Give the position of every Plasmodium parasite visible.
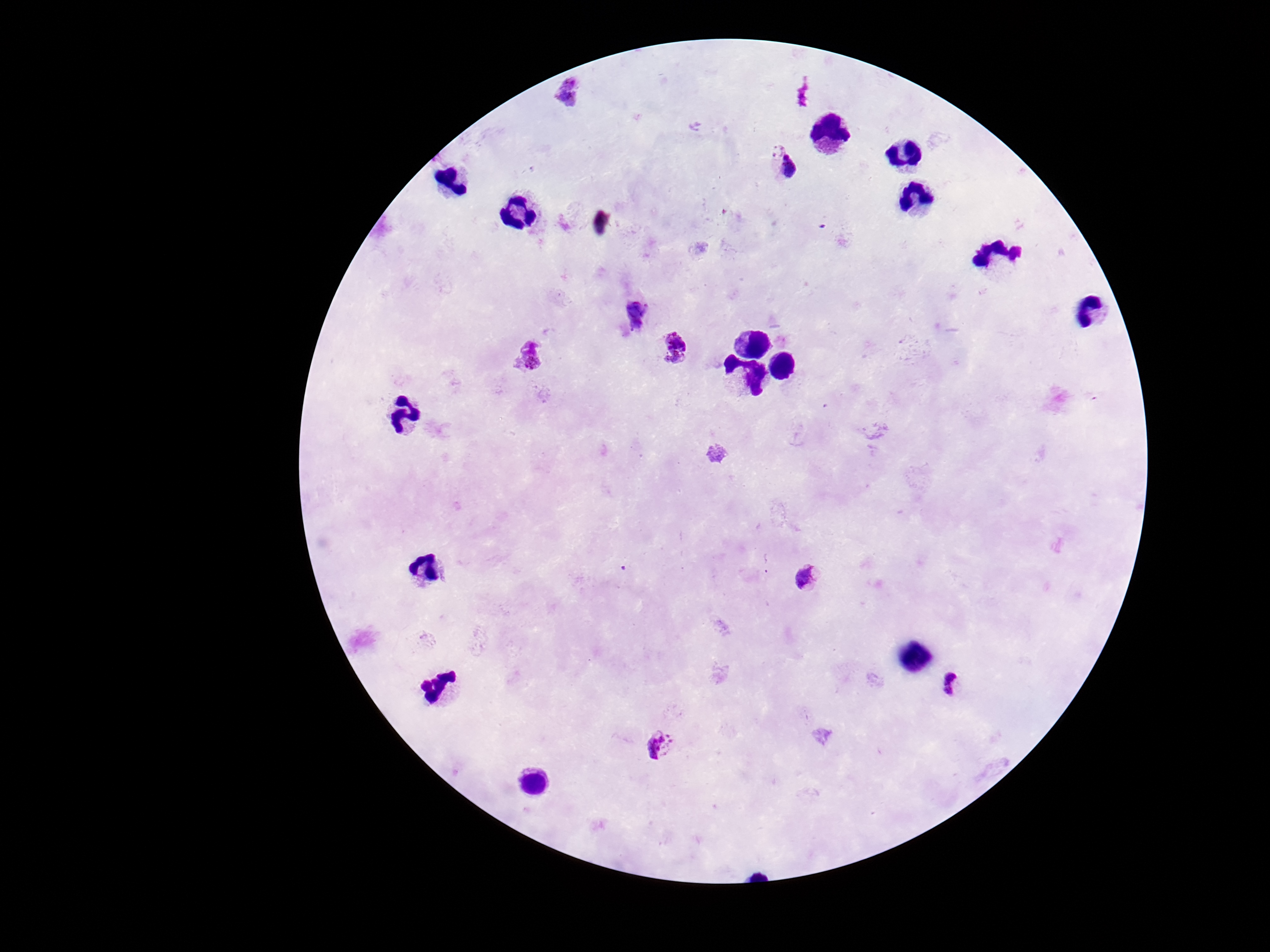
Approximate centers as {x, y} in pixels.
Plasmodium parasites: {566, 91}, {777, 149}, {786, 170}, {635, 314}, {676, 347}, {529, 360}, {811, 577}, {955, 688}, {661, 746}.

Summary:
  - Patient malaria status: positive
  - Stain: Giemsa
  - Field of view: single
  - Magnification: 100x
  - Image size: 1270×952 pixels
  - Capture: smartphone camera through the microscope eyepiece
  - Preparation: thick blood smear